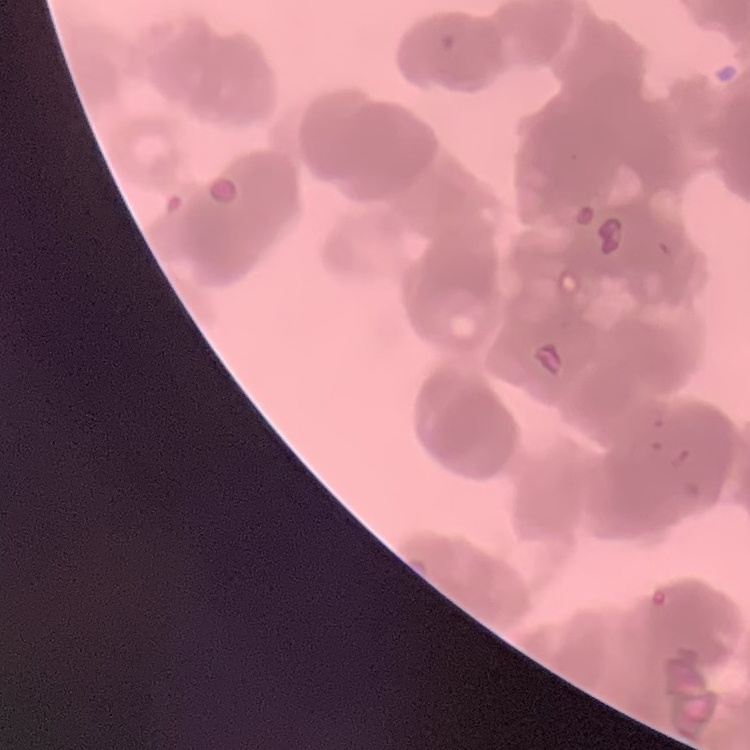

{
  "erythrocyte_morphology": "rouleaux formation",
  "image_type": "square crop of a larger photomicrograph",
  "preparation": "thin peripheral smear",
  "stain": "Field's or Giemsa"
}